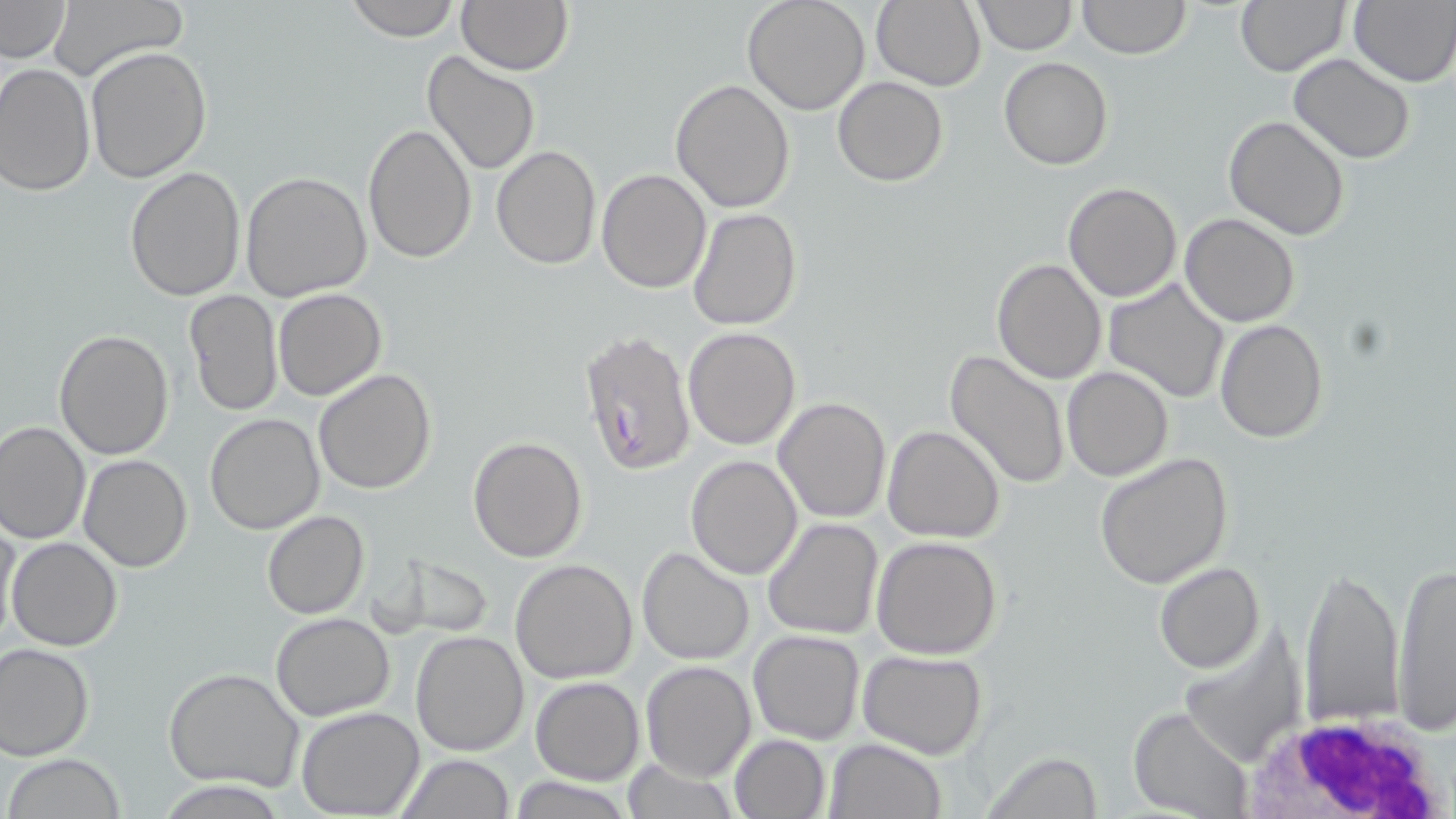

Summary:
  - Coordinate format: approximate bounding boxes as (x1, y1, x2, y2) in pixels
  - White blood cell locations: (1223, 713, 1450, 815)
  - Uninfected red blood cell locations: (344, 0, 460, 41), (870, 0, 986, 90), (972, 0, 1075, 54), (1078, 0, 1190, 59), (1235, 0, 1351, 75), (0, 1, 73, 64), (458, 1, 573, 74), (742, 1, 871, 115), (51, 2, 182, 81), (1348, 2, 1456, 85), (85, 45, 212, 183), (421, 52, 540, 176), (1290, 53, 1417, 164), (999, 58, 1113, 170), (0, 63, 96, 195), (833, 76, 948, 186), (670, 79, 796, 212), (1224, 116, 1351, 240), (362, 123, 477, 263), (490, 144, 602, 270), (125, 166, 245, 301), (596, 167, 711, 293), (240, 170, 372, 301), (1063, 180, 1183, 301), (688, 207, 802, 331), (1180, 213, 1300, 327), (991, 259, 1107, 384), (1103, 278, 1231, 405), (273, 288, 386, 402), (184, 289, 283, 417), (1215, 318, 1327, 443), (683, 326, 801, 448), (54, 330, 173, 460), (944, 350, 1071, 489), (1062, 366, 1174, 481), (313, 369, 437, 495), (773, 395, 891, 522), (204, 413, 324, 534), (1, 421, 90, 546), (881, 425, 1006, 543), (468, 436, 588, 563), (1095, 451, 1234, 588), (79, 454, 194, 572), (685, 455, 802, 579), (261, 510, 369, 619), (762, 516, 885, 640), (0, 519, 20, 646), (872, 535, 1003, 659), (8, 537, 123, 653), (637, 547, 755, 665), (380, 550, 498, 639), (510, 559, 639, 683), (1390, 560, 1455, 734), (1156, 561, 1264, 673), (1299, 566, 1409, 727), (272, 613, 395, 720), (409, 629, 529, 756), (749, 630, 864, 745), (0, 642, 95, 760), (857, 649, 987, 759), (640, 660, 755, 782), (165, 667, 305, 792), (531, 676, 644, 785), (296, 705, 424, 817), (1130, 707, 1254, 819), (730, 733, 830, 818), (824, 738, 945, 819), (981, 752, 1105, 817), (397, 753, 514, 818), (3, 755, 127, 818), (619, 760, 740, 816), (511, 778, 635, 817)
  - Plasmodium falciparum-infected red blood cell locations: (579, 331, 699, 476)
  - Slide-level diagnosis: Plasmodium falciparum
  - Stain: May-Grünwald-Giemsa
  - Field of view: single
  - Magnification: 1000x
  - Preparation: thin blood smear
  - Modality: light microscopy
  - Image size: 1456×819 pixels